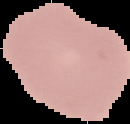

The area outside the segmented cell region is set to black. Malaria status: uninfected. Image is 130×124 pixels. From a thin blood smear.